Describe the morphology of the red blood cells.
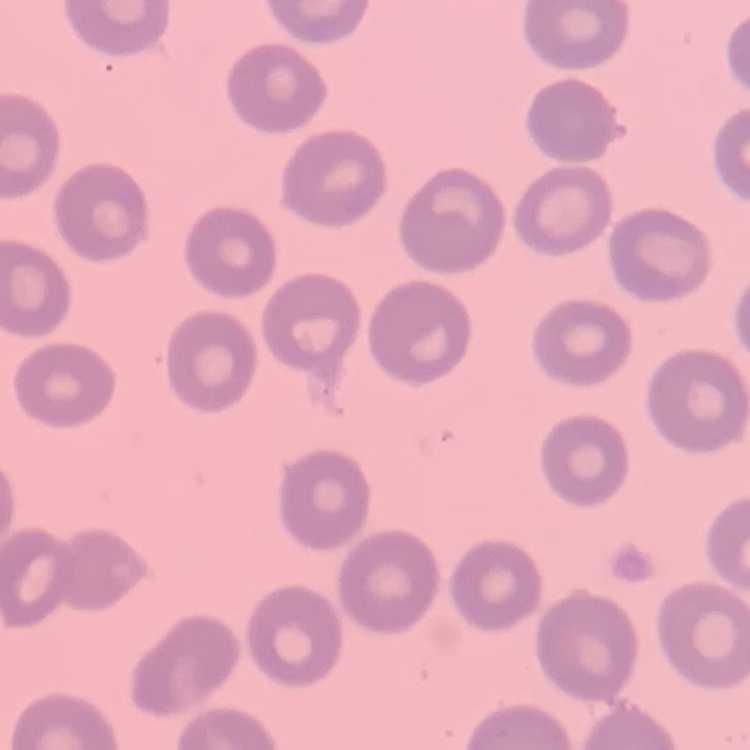

No rouleaux formation.

stain: Field's or Giemsa
preparation: thin peripheral smear
image_type: square crop of a larger photomicrograph